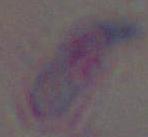
magnification = 1000x
modality = photomicrograph
identification = Toxoplasma gondii